Identify the parasite.
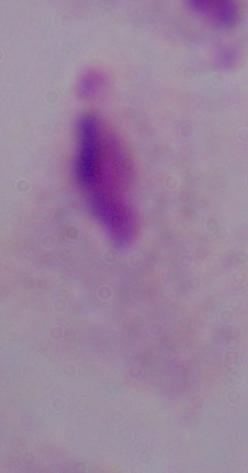

This is a trichomonad.

Micrograph. 1000x magnification.